Name the parasite shown.
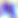
Toxoplasma gondii.

magnification = 400x
modality = photomicrograph